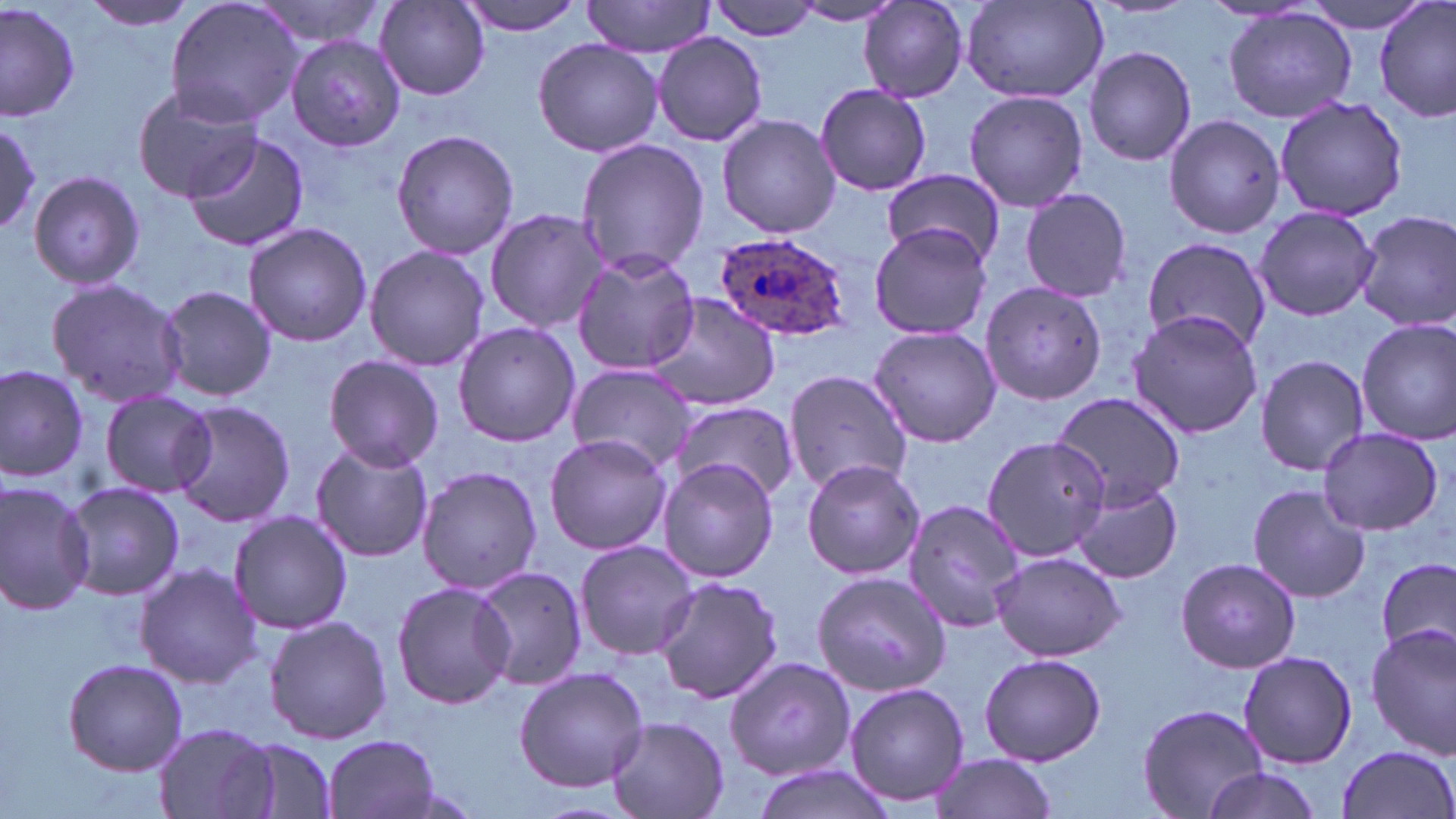

Summary:
  - Coordinate format: approximate bounding boxes as [x1, y1, x2, y2] in pixels
  - Uninfected red blood cell locations: [79, 0, 199, 32], [165, 0, 302, 129], [249, 0, 395, 49], [456, 0, 588, 36], [583, 0, 715, 59], [1300, 0, 1434, 31], [0, 1, 80, 122], [857, 1, 970, 104], [1376, 1, 1456, 123], [375, 2, 490, 99], [703, 2, 823, 41], [793, 2, 907, 25], [960, 2, 1109, 103], [1223, 10, 1357, 124], [283, 31, 407, 153], [652, 32, 769, 147], [532, 37, 663, 158], [1083, 45, 1197, 167], [815, 84, 931, 197], [132, 87, 260, 203], [963, 91, 1089, 211], [1273, 93, 1410, 225], [0, 112, 41, 240], [1161, 113, 1288, 241], [718, 114, 841, 237], [391, 129, 518, 260], [184, 131, 310, 254], [576, 137, 708, 276], [882, 168, 1006, 267], [27, 170, 146, 290], [1018, 187, 1133, 303], [1254, 206, 1381, 322], [482, 208, 607, 334], [1354, 211, 1456, 335], [867, 222, 992, 341], [244, 223, 372, 348], [1139, 236, 1272, 353], [364, 244, 490, 371], [572, 249, 698, 375], [45, 278, 189, 407], [977, 281, 1107, 406], [157, 284, 278, 401], [646, 292, 781, 410], [1127, 309, 1263, 441], [1356, 318, 1456, 445], [453, 322, 581, 447], [869, 325, 999, 448], [1255, 354, 1370, 475], [323, 355, 443, 470], [565, 362, 698, 472], [0, 363, 90, 482], [783, 369, 915, 496], [100, 391, 217, 496], [1048, 391, 1185, 512], [169, 400, 297, 528], [669, 400, 799, 503], [1315, 427, 1444, 537], [543, 432, 671, 556], [980, 434, 1109, 562], [310, 440, 434, 564], [657, 458, 778, 583], [801, 459, 924, 578], [416, 466, 544, 594], [0, 478, 97, 615], [64, 480, 186, 603], [1072, 482, 1183, 584], [1247, 484, 1371, 604], [900, 496, 1028, 632], [227, 510, 354, 635], [574, 538, 701, 661], [990, 552, 1126, 662], [1173, 557, 1303, 675], [1376, 557, 1455, 660], [134, 565, 261, 687], [471, 566, 586, 690], [812, 571, 951, 696], [654, 574, 782, 705], [391, 581, 515, 709], [265, 615, 392, 744], [1364, 624, 1456, 755], [1236, 649, 1360, 769], [978, 651, 1107, 766], [724, 655, 855, 780], [62, 657, 188, 776], [514, 665, 649, 791], [841, 681, 970, 809], [1135, 703, 1268, 819], [606, 715, 730, 819], [154, 723, 278, 819], [321, 734, 446, 819], [233, 737, 341, 819], [1336, 743, 1455, 819], [926, 754, 1060, 819], [750, 763, 899, 819], [1191, 765, 1324, 819]
  - Plasmodium ovale-infected red blood cell locations: [712, 231, 854, 342]
  - Slide-level diagnosis: Plasmodium ovale
  - Preparation: thin blood smear
  - Field of view: one of a larger specimen
  - Image size: 1456×819 pixels
  - Magnification: 1000x
  - Stain: May-Grünwald-Giemsa
  - Modality: optical microscopy